Give the position of every Plasmodium parasite visible.
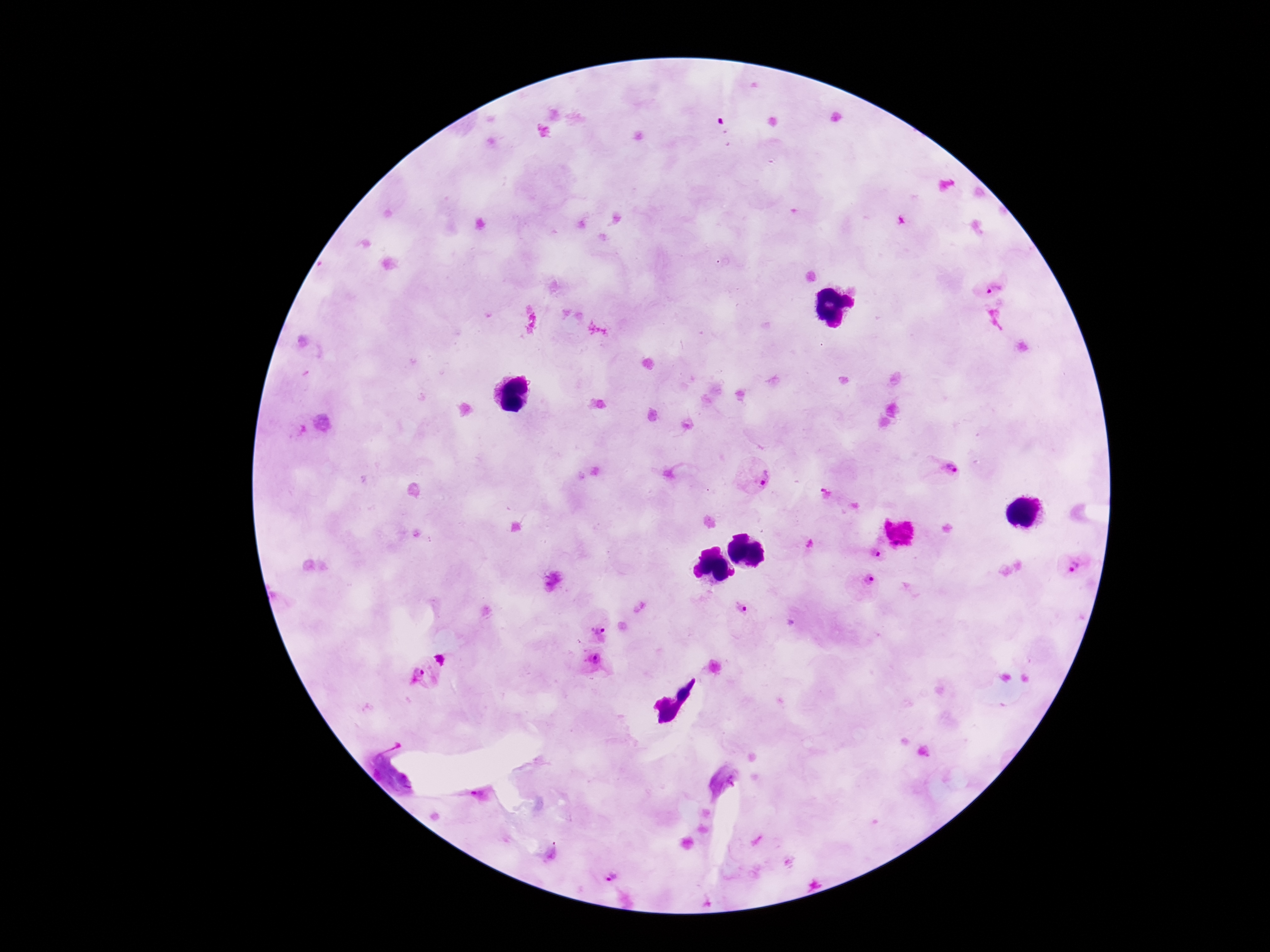
Approximate centers as {x, y} in pixels.
Plasmodium parasites: {991, 283}, {941, 471}, {755, 475}, {825, 496}, {803, 545}, {869, 553}, {1074, 568}, {866, 589}, {741, 607}, {598, 632}, {590, 661}, {421, 674}, {606, 873}.

Patient malaria status: infected. 100x magnification. Image is 1270×952 pixels. Thick peripheral-blood smear. Photographed through the microscope eyepiece with a smartphone camera. Giemsa stain. Single field of view.